Evaluate for parasitized red blood cells.
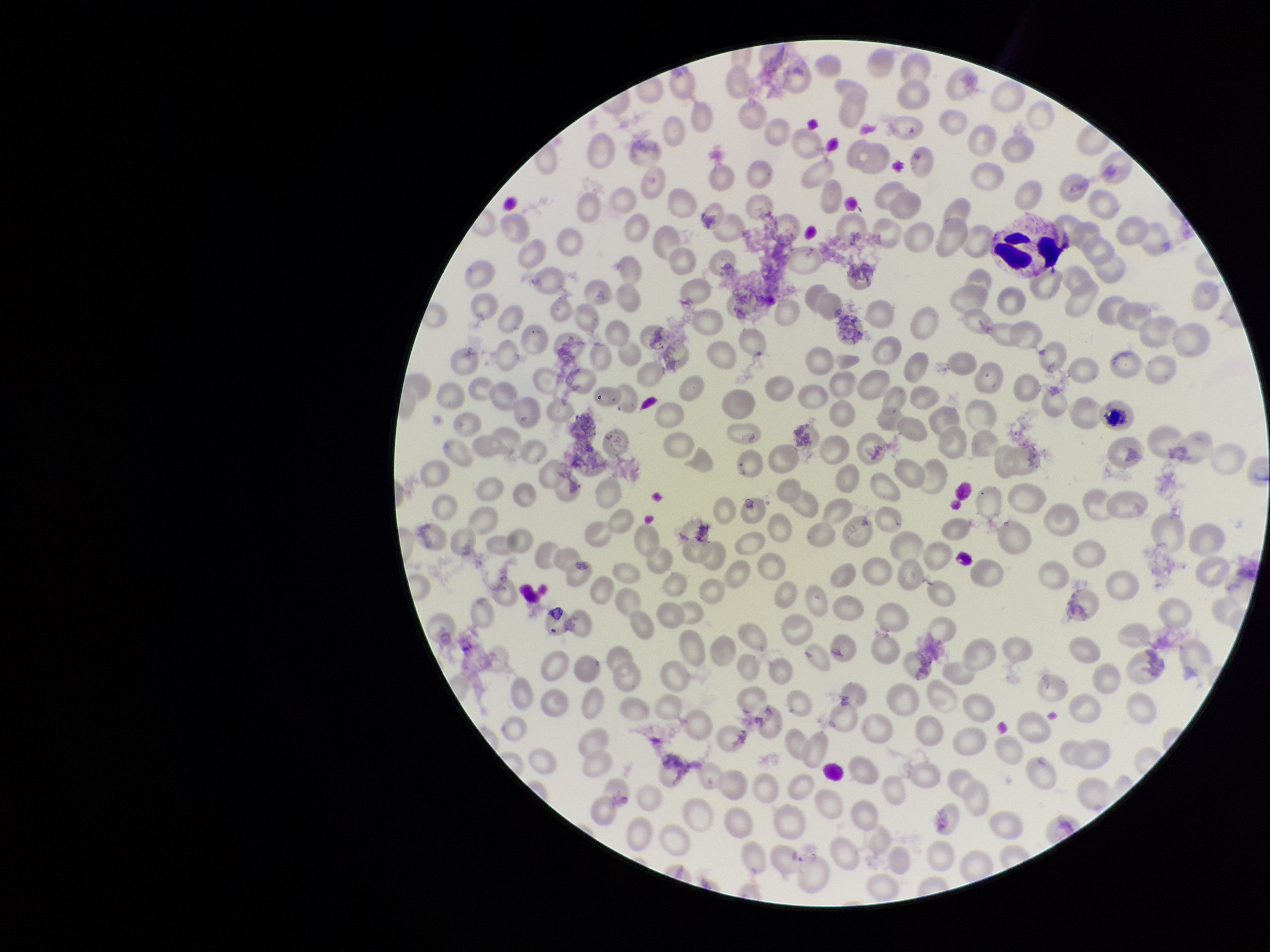
None seen.

Summary:
  - Species reported for this patient: Plasmodium vivax
  - Red blood cell count: 247
  - Preparation: thin
  - Parasitized red blood cell count: 0
  - Capture: smartphone photograph through the microscope eyepiece
  - Field of view: one from this slide
  - Image size: 1270×952 pixels
  - Patient malaria status: positive
  - Stain: Giemsa